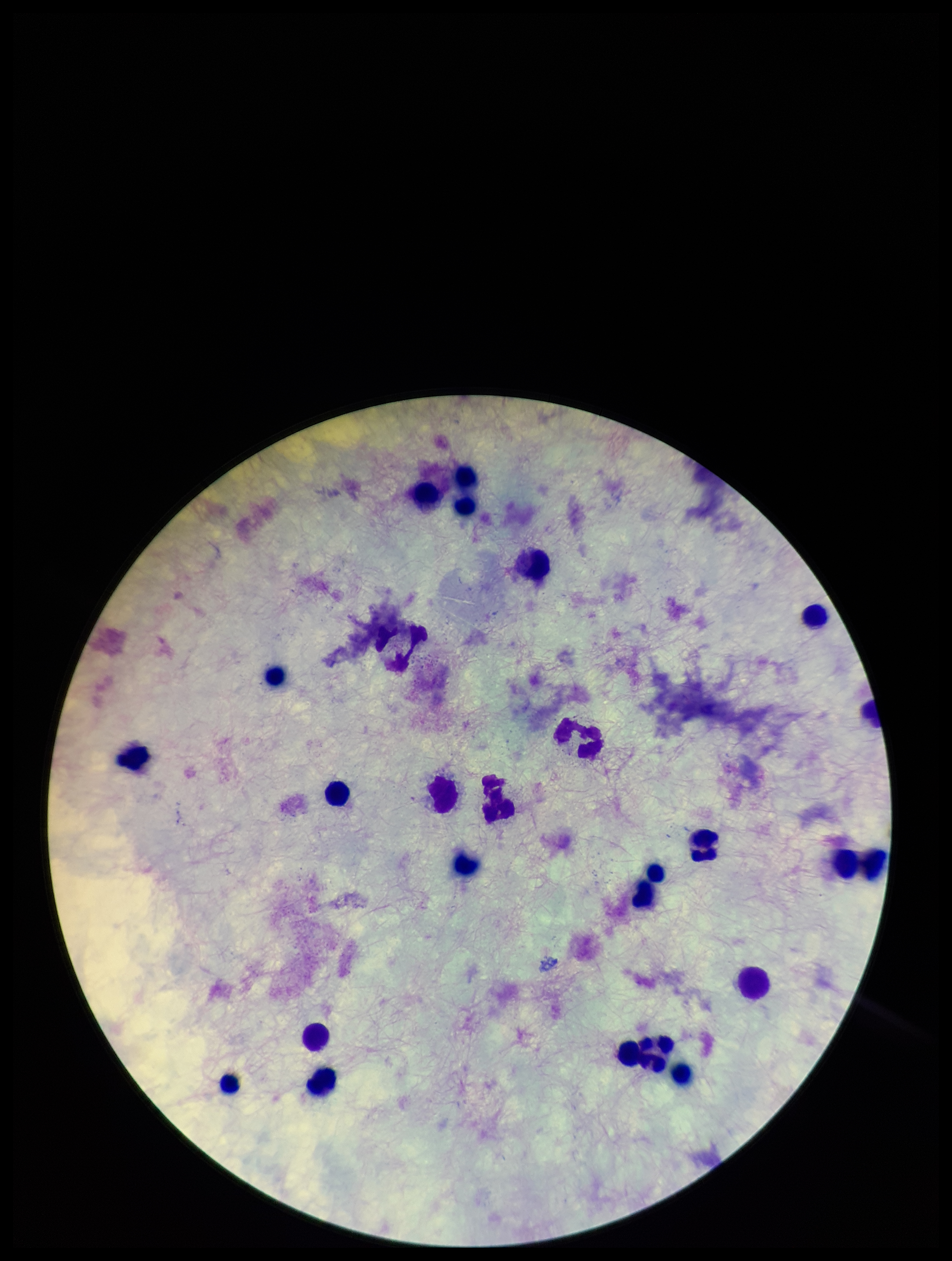
Preparation: thick. Patient malaria status: negative. Image is 952×1261 pixels. Plasmodium parasites: none seen. Parasite count: 0. Leukocyte count: 23. Smartphone photograph taken through the eyepiece of a microscope. One field from this slide. Stained with Giemsa.